Assess this cell for malaria.
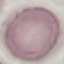

Uninfected.

capture = smartphone through the microscope eyepiece
image type = cell patch, automatically extracted from a larger field of view and resized to 64 × 64 pixels
stain = Giemsa
preparation = thin blood film